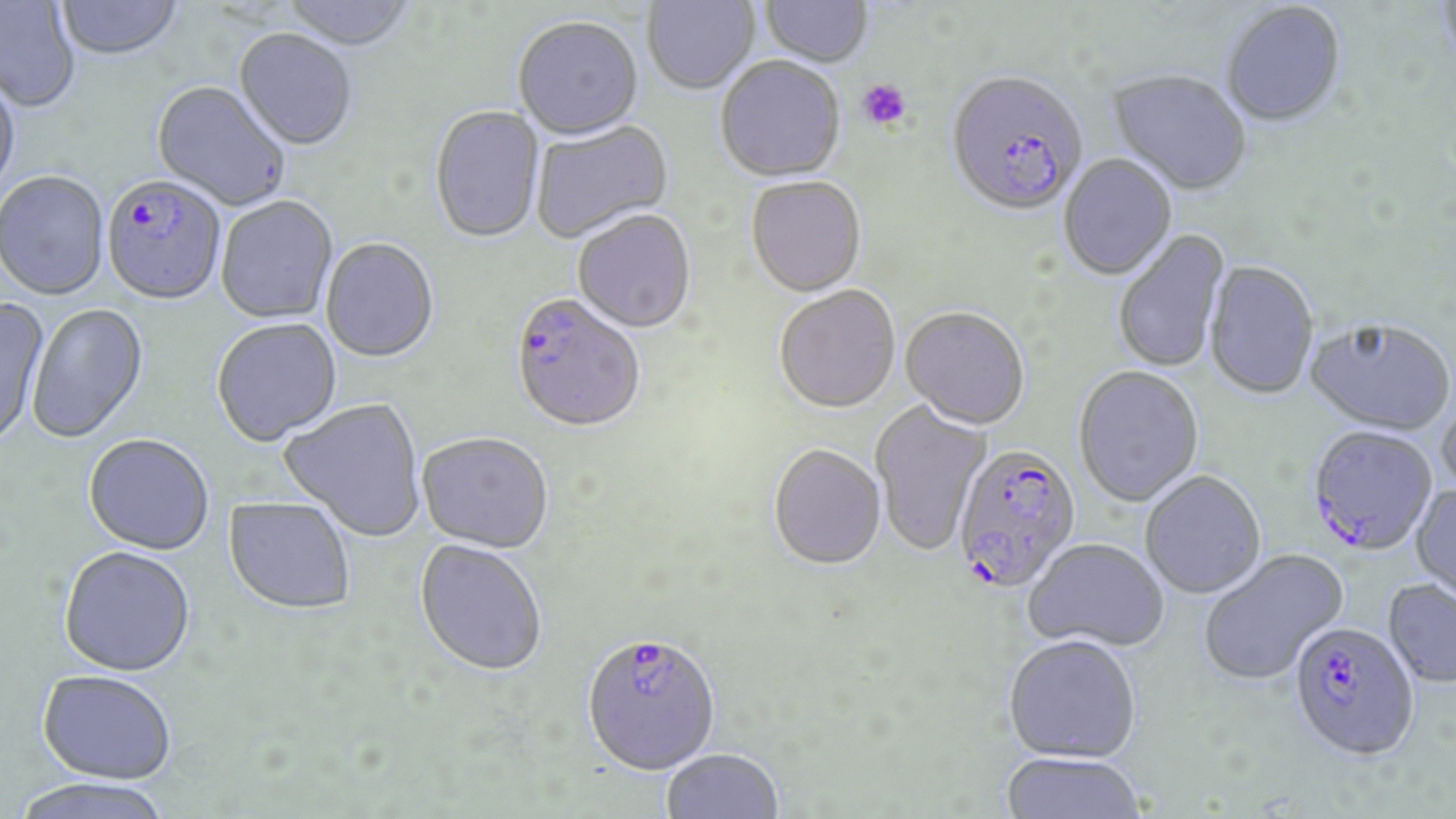
Approximate bounding boxes as [x1, y1, x2, y2] in pixels. Platelet locations: [856, 79, 911, 131]. Uninfected red blood cell locations: [55, 0, 185, 62], [280, 0, 418, 53], [643, 0, 760, 96], [760, 1, 874, 70], [0, 2, 82, 114], [1221, 3, 1347, 130], [512, 19, 644, 142], [233, 30, 358, 153], [715, 59, 846, 185], [0, 70, 21, 201], [1107, 71, 1251, 199], [152, 82, 290, 212], [429, 106, 545, 246], [531, 121, 674, 245], [1059, 155, 1177, 281], [0, 172, 110, 301], [745, 179, 866, 299], [216, 197, 338, 325], [573, 212, 697, 335], [1113, 229, 1231, 374], [320, 239, 440, 365], [1204, 262, 1319, 401], [774, 287, 901, 416], [0, 295, 50, 451], [26, 304, 149, 445], [900, 309, 1029, 432], [211, 319, 342, 448], [1304, 319, 1455, 438], [1073, 367, 1204, 508], [280, 398, 426, 542], [1436, 398, 1456, 505], [870, 400, 992, 558], [83, 434, 215, 556], [417, 434, 553, 555], [768, 446, 886, 573], [1140, 471, 1266, 599], [1410, 484, 1456, 605], [222, 497, 355, 616], [1023, 539, 1170, 653], [414, 540, 547, 678], [58, 546, 196, 677], [1198, 548, 1348, 686], [1383, 579, 1456, 688], [1003, 635, 1141, 762], [37, 669, 178, 783], [660, 748, 784, 818], [999, 752, 1147, 819], [8, 776, 177, 819]. Plasmodium falciparum-infected red blood cell locations: [945, 74, 1087, 220], [102, 176, 227, 307], [509, 295, 645, 437], [1307, 427, 1437, 557], [952, 446, 1082, 596], [1289, 621, 1419, 760], [580, 633, 720, 776]. Slide-level diagnosis: Plasmodium falciparum. Captured at 1000x magnification. Image is 1456×819 pixels. Optical microscopy. One field of a larger specimen. May-Grünwald-Giemsa-stained preparation. Thin blood film.